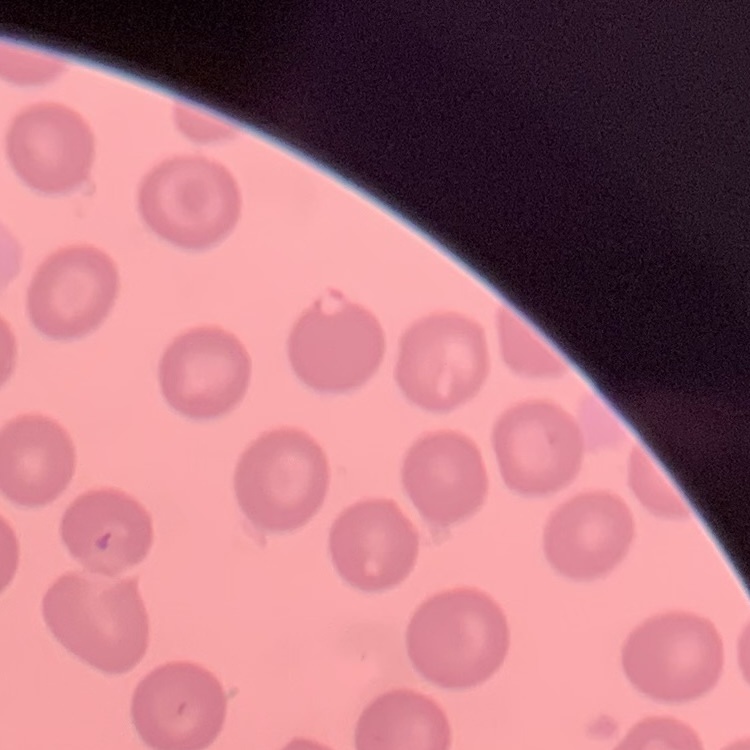
erythrocyte_morphology: no rouleaux formation
image_type: one tile cut from a larger photomicrograph
preparation: thin blood smear
stain: Field's or Giemsa